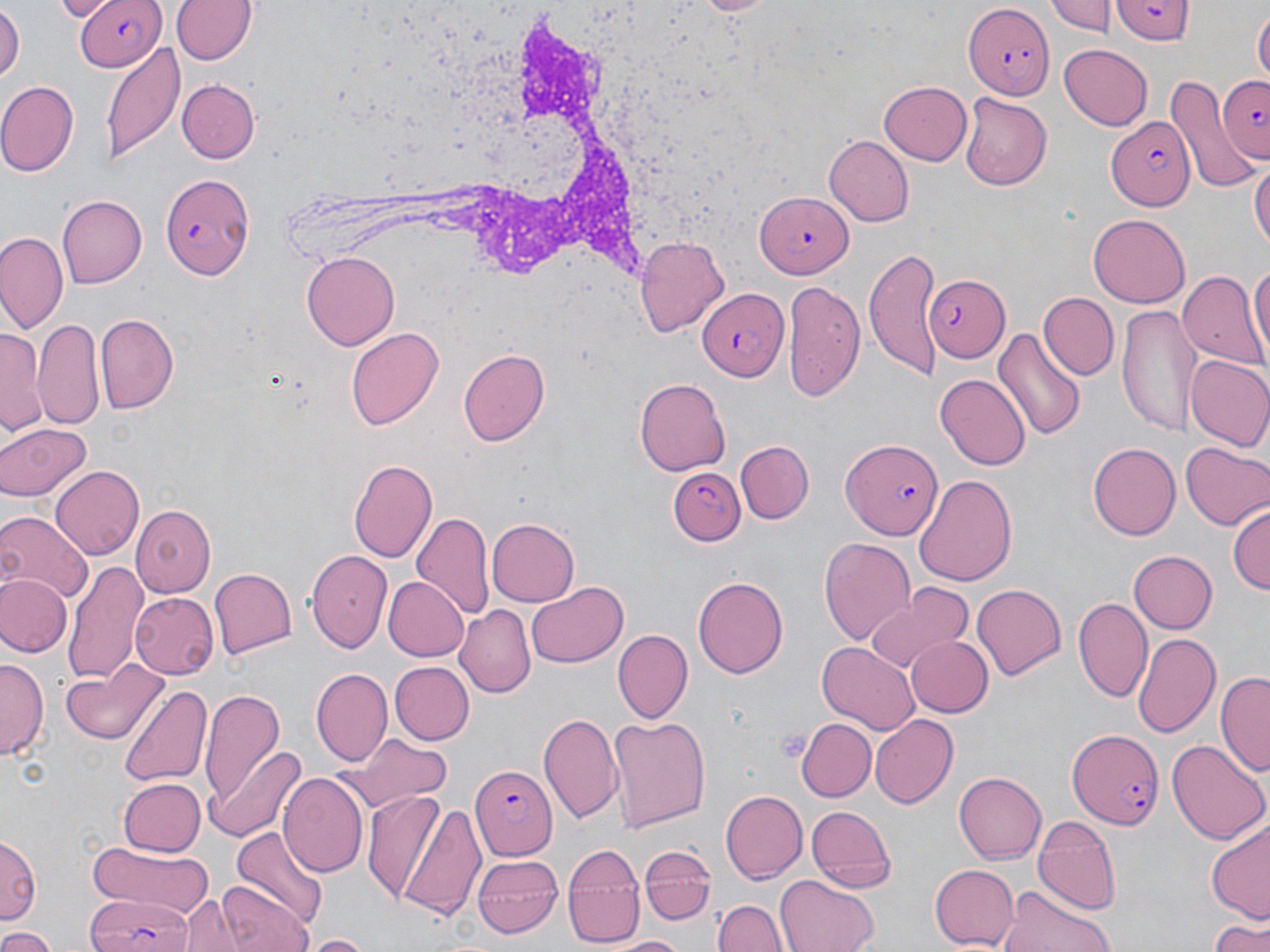 Approximate bounding boxes as (x1, y1, x2, y2) in pixels. Plasmodium falciparum-infected red blood cell locations: (73, 0, 166, 71), (1113, 1, 1192, 46), (962, 3, 1053, 97), (1216, 73, 1270, 164), (1106, 112, 1198, 209), (159, 171, 258, 278), (752, 191, 850, 277), (927, 273, 1011, 362), (695, 287, 786, 380), (840, 436, 943, 539), (668, 466, 745, 547), (1065, 727, 1167, 830), (472, 764, 559, 856), (83, 894, 194, 952). Uninfected red blood cell locations: (171, 0, 255, 67), (692, 0, 775, 17), (1047, 0, 1111, 37), (0, 4, 22, 84), (1253, 9, 1269, 86), (101, 41, 185, 164), (1058, 43, 1153, 129), (1167, 76, 1261, 190), (176, 78, 259, 164), (878, 79, 972, 167), (0, 81, 80, 176), (960, 92, 1051, 189), (824, 134, 912, 226), (1251, 154, 1269, 257), (56, 195, 146, 288), (1089, 213, 1190, 307), (0, 232, 66, 332), (635, 235, 731, 337), (864, 247, 938, 379), (299, 250, 400, 350), (1249, 258, 1270, 365), (1179, 271, 1263, 367), (782, 282, 864, 402), (1040, 292, 1118, 380), (1116, 305, 1200, 434), (95, 313, 178, 413), (34, 319, 105, 434), (995, 324, 1085, 440), (346, 326, 444, 431), (1, 328, 45, 437), (459, 348, 551, 446), (1184, 355, 1270, 454), (936, 373, 1031, 470), (633, 378, 731, 475), (0, 422, 93, 503), (734, 441, 813, 524), (1087, 441, 1181, 541), (1182, 442, 1269, 530), (349, 459, 438, 562), (51, 464, 145, 558), (913, 473, 1018, 588), (1229, 503, 1269, 598), (131, 504, 217, 596), (0, 510, 93, 605), (411, 513, 494, 621), (484, 518, 578, 607), (818, 536, 915, 646), (1126, 548, 1216, 635), (307, 551, 391, 653), (63, 562, 146, 686), (208, 567, 296, 658), (1, 572, 71, 657), (693, 574, 787, 683), (383, 576, 468, 662), (527, 581, 628, 667), (971, 582, 1067, 682), (867, 583, 974, 673), (131, 591, 220, 678), (1074, 594, 1151, 701), (456, 607, 536, 698), (615, 630, 694, 722), (1132, 632, 1221, 738), (904, 636, 993, 718), (818, 641, 920, 735), (1, 658, 46, 761), (63, 661, 169, 745), (391, 663, 474, 744), (312, 667, 392, 766), (1216, 670, 1270, 776), (119, 683, 211, 788), (198, 685, 289, 817), (539, 710, 625, 828), (868, 711, 958, 805), (606, 713, 712, 834), (795, 716, 875, 800), (350, 736, 452, 806), (1169, 738, 1267, 846), (211, 748, 306, 841), (956, 770, 1046, 864), (278, 771, 369, 878), (118, 778, 205, 856), (361, 788, 449, 903), (722, 791, 809, 882), (394, 798, 489, 919), (805, 805, 896, 893), (1032, 815, 1120, 914), (1206, 816, 1270, 920), (231, 827, 328, 931), (0, 834, 39, 925), (87, 840, 216, 917), (639, 841, 718, 922), (562, 843, 644, 947), (474, 854, 563, 937), (929, 864, 1019, 950), (775, 875, 879, 952), (216, 880, 312, 952), (996, 889, 1117, 952), (180, 896, 248, 951), (714, 898, 787, 952), (1207, 915, 1270, 952), (0, 928, 56, 952), (302, 934, 377, 952), (612, 936, 689, 952). Platelet locations: (771, 727, 811, 764). Slide-level diagnosis: Plasmodium falciparum. Thin blood film. May-Grünwald-Giemsa stain. 1000x magnification. One field of a larger specimen. Image is 1270×952 pixels. Light microscopy.